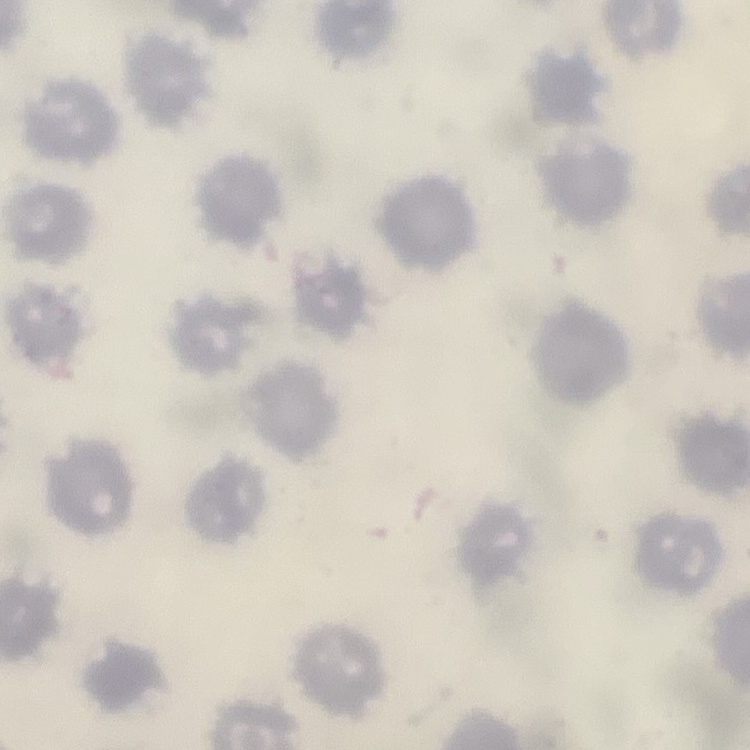
Summary:
  - Red blood cell morphology: no rouleaux formation
  - Image type: square crop of a larger photomicrograph
  - Preparation: thin peripheral smear
  - Stain: Field's or Giemsa